Identify the cell.
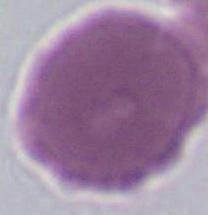

An erythrocyte.

magnification = 1000x
modality = photomicrograph